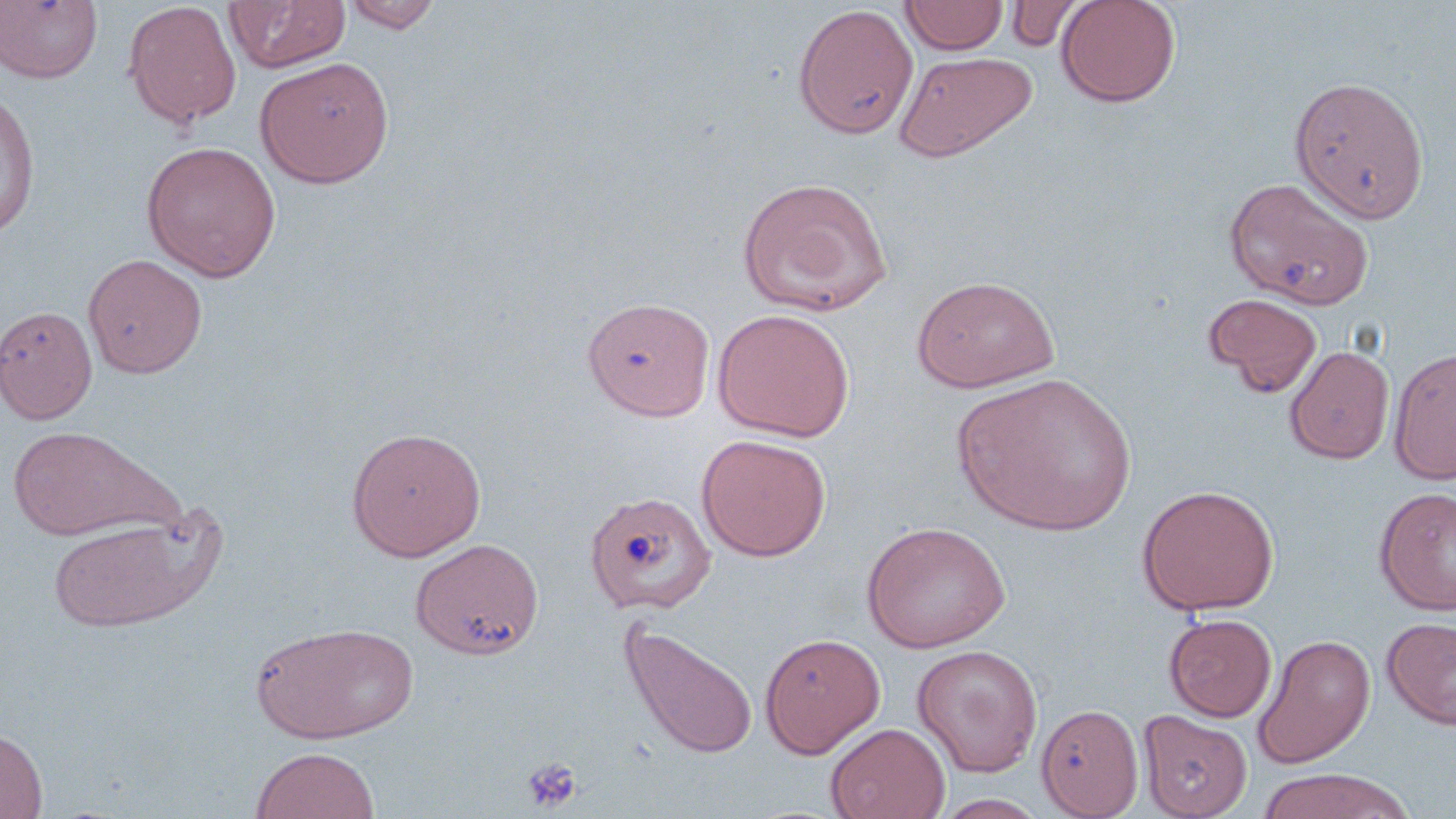

Approximate bounding boxes as named x1/y1/x2/y2 corners in pixels. Uninfected red blood cell locations: (x1=223, y1=0, x2=350, y2=74), (x1=900, y1=0, x2=1009, y2=55), (x1=1055, y1=0, x2=1181, y2=108), (x1=1, y1=1, x2=103, y2=83), (x1=122, y1=1, x2=242, y2=129), (x1=343, y1=1, x2=443, y2=32), (x1=1005, y1=1, x2=1088, y2=52), (x1=794, y1=5, x2=919, y2=141), (x1=894, y1=50, x2=1037, y2=162), (x1=254, y1=56, x2=394, y2=188), (x1=1288, y1=75, x2=1430, y2=223), (x1=0, y1=87, x2=39, y2=239), (x1=142, y1=141, x2=282, y2=281), (x1=736, y1=175, x2=894, y2=317), (x1=1224, y1=176, x2=1374, y2=309), (x1=83, y1=253, x2=208, y2=379), (x1=912, y1=275, x2=1061, y2=393), (x1=1203, y1=293, x2=1323, y2=397), (x1=582, y1=296, x2=715, y2=420), (x1=0, y1=305, x2=97, y2=425), (x1=711, y1=308, x2=855, y2=441), (x1=1284, y1=345, x2=1395, y2=464), (x1=1389, y1=346, x2=1456, y2=485), (x1=954, y1=372, x2=1137, y2=536), (x1=5, y1=425, x2=174, y2=542), (x1=346, y1=426, x2=486, y2=562), (x1=695, y1=434, x2=831, y2=562), (x1=1136, y1=484, x2=1279, y2=615), (x1=1374, y1=486, x2=1456, y2=616), (x1=584, y1=489, x2=717, y2=616), (x1=45, y1=514, x2=213, y2=633), (x1=861, y1=520, x2=1010, y2=654), (x1=410, y1=537, x2=544, y2=659), (x1=1163, y1=613, x2=1277, y2=722), (x1=1382, y1=616, x2=1456, y2=730), (x1=618, y1=618, x2=759, y2=761), (x1=250, y1=621, x2=417, y2=744), (x1=759, y1=632, x2=885, y2=758), (x1=1252, y1=633, x2=1376, y2=769), (x1=911, y1=644, x2=1043, y2=778), (x1=1036, y1=704, x2=1144, y2=818), (x1=1138, y1=709, x2=1252, y2=819), (x1=825, y1=723, x2=950, y2=819), (x1=0, y1=727, x2=48, y2=819), (x1=249, y1=746, x2=381, y2=819), (x1=1254, y1=769, x2=1416, y2=819), (x1=932, y1=793, x2=1051, y2=818). Platelet locations: (x1=521, y1=757, x2=583, y2=812). Slide-level diagnosis: no evidence of blood parasites. Image is 1456×819 pixels. May-Grünwald-Giemsa stain. Optical microscopy. Thin blood film. 1000x magnification. One field of a larger specimen.